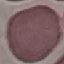

result = no malaria parasites seen
stain = Giemsa
preparation = thin blood smear
image type = automatically extracted cell patch, resized to 64 × 64 pixels
capture = smartphone camera at the microscope eyepiece